Locate and identify every blood parasite.
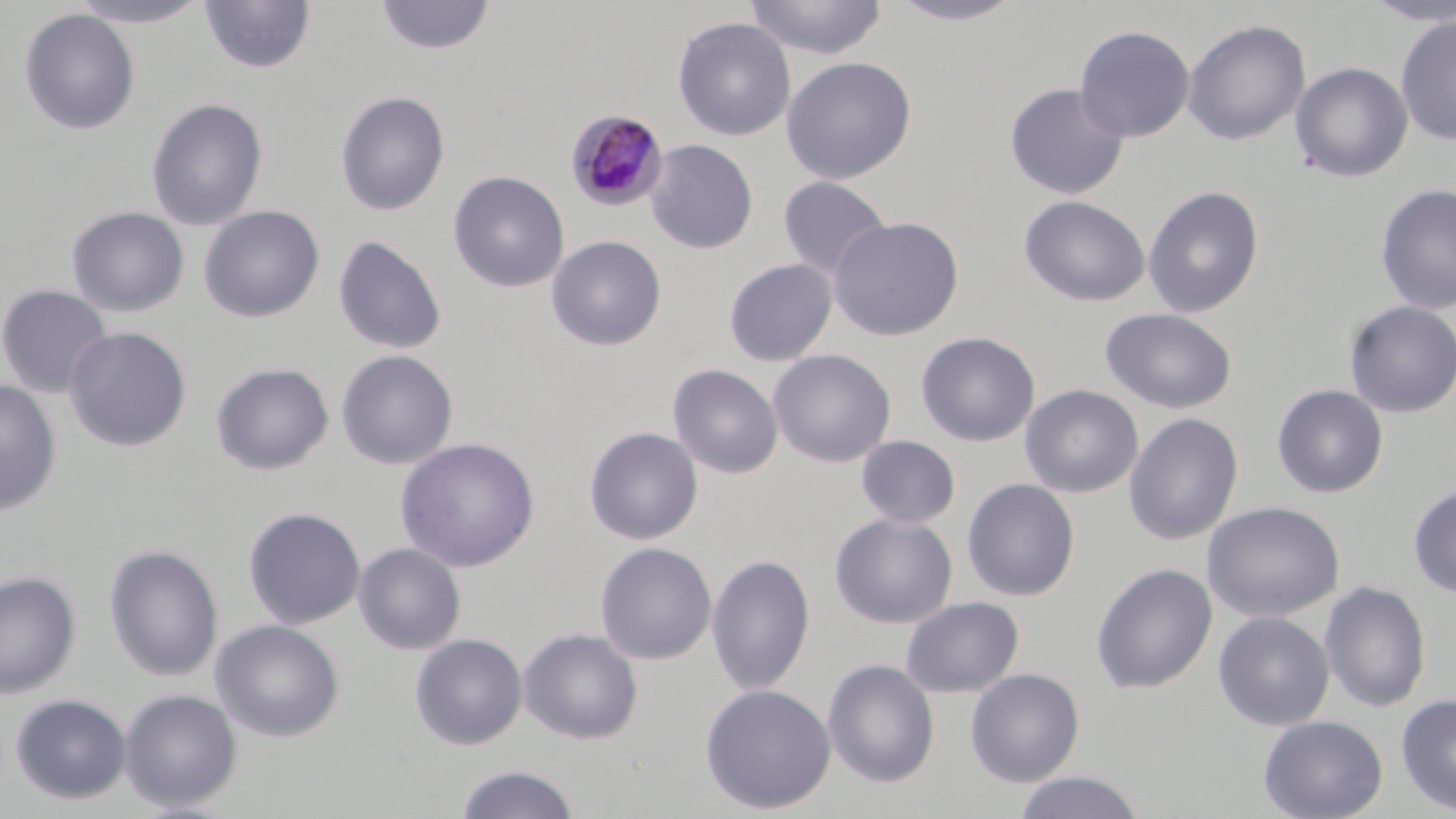
Approximate bounding boxes as [x1, y1, x2, y2] in pixels.
Plasmodium malariae-infected red blood cells: [565, 109, 669, 210].
No Plasmodium falciparum, Plasmodium ovale, Plasmodium vivax, Babesia divergens, or Trypanosoma brucei observed.

slide_level_diagnosis: Plasmodium malariae
preparation: thin blood film
image_size: 1456×819 pixels
modality: optical microscopy
uninfected_red_blood_cell_locations: 'approximate bounding boxes as [x1, y1, x2, y2] in pixels: [68, 0, 213, 28], [375, 0, 496, 55], [744, 0, 888, 60], [886, 0, 1028, 26], [1361, 0, 1456, 26], [199, 1, 316, 75], [18, 9, 140, 135], [1395, 15, 1456, 145], [672, 17, 796, 142], [1183, 19, 1311, 146], [1074, 24, 1195, 143], [781, 56, 917, 184], [1289, 62, 1413, 183], [1004, 83, 1129, 200], [335, 90, 450, 216], [146, 98, 268, 231], [646, 139, 759, 254], [448, 170, 569, 293], [777, 176, 892, 280], [1375, 183, 1456, 316], [1142, 185, 1265, 318], [1019, 195, 1150, 307], [199, 205, 324, 323], [66, 206, 189, 317], [828, 215, 964, 341], [546, 235, 667, 351], [333, 236, 447, 354], [723, 259, 837, 366], [0, 284, 113, 398], [1344, 301, 1456, 418], [1100, 307, 1238, 414], [63, 326, 192, 452], [916, 332, 1041, 447], [767, 349, 896, 467], [336, 350, 458, 469], [210, 362, 334, 475], [668, 364, 783, 479], [0, 380, 62, 516], [1020, 384, 1143, 498], [1272, 384, 1389, 499], [1123, 413, 1244, 546], [584, 426, 703, 545], [856, 435, 960, 528], [395, 437, 540, 573], [962, 478, 1081, 601], [1408, 484, 1456, 598], [1202, 501, 1345, 623], [243, 507, 365, 629], [829, 512, 958, 628], [353, 542, 466, 655], [595, 542, 717, 665], [103, 543, 223, 682], [706, 555, 815, 695], [1090, 563, 1217, 694], [0, 570, 81, 698], [1318, 580, 1431, 713], [901, 597, 1024, 698], [1212, 611, 1335, 730], [210, 619, 344, 742], [518, 627, 643, 744], [409, 633, 528, 750], [822, 659, 940, 787], [965, 668, 1085, 787], [699, 683, 836, 814], [118, 688, 242, 812], [9, 693, 132, 805], [1395, 693, 1456, 815], [1258, 715, 1388, 819], [454, 764, 581, 819], [1012, 770, 1145, 819]'
stain: May-Grünwald-Giemsa
magnification: 1000x
field_of_view: one of a larger specimen